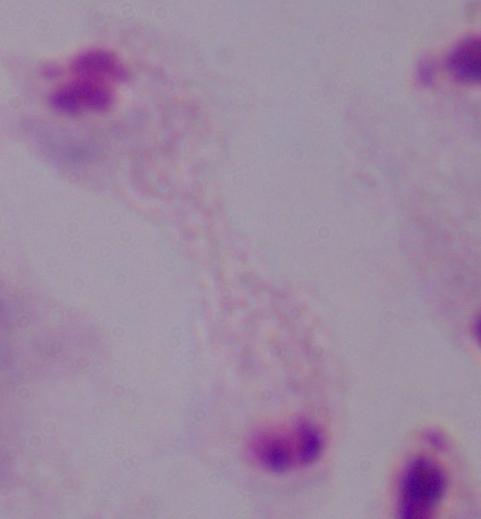
magnification = 1000x
identification = trichomonad
modality = photomicrograph